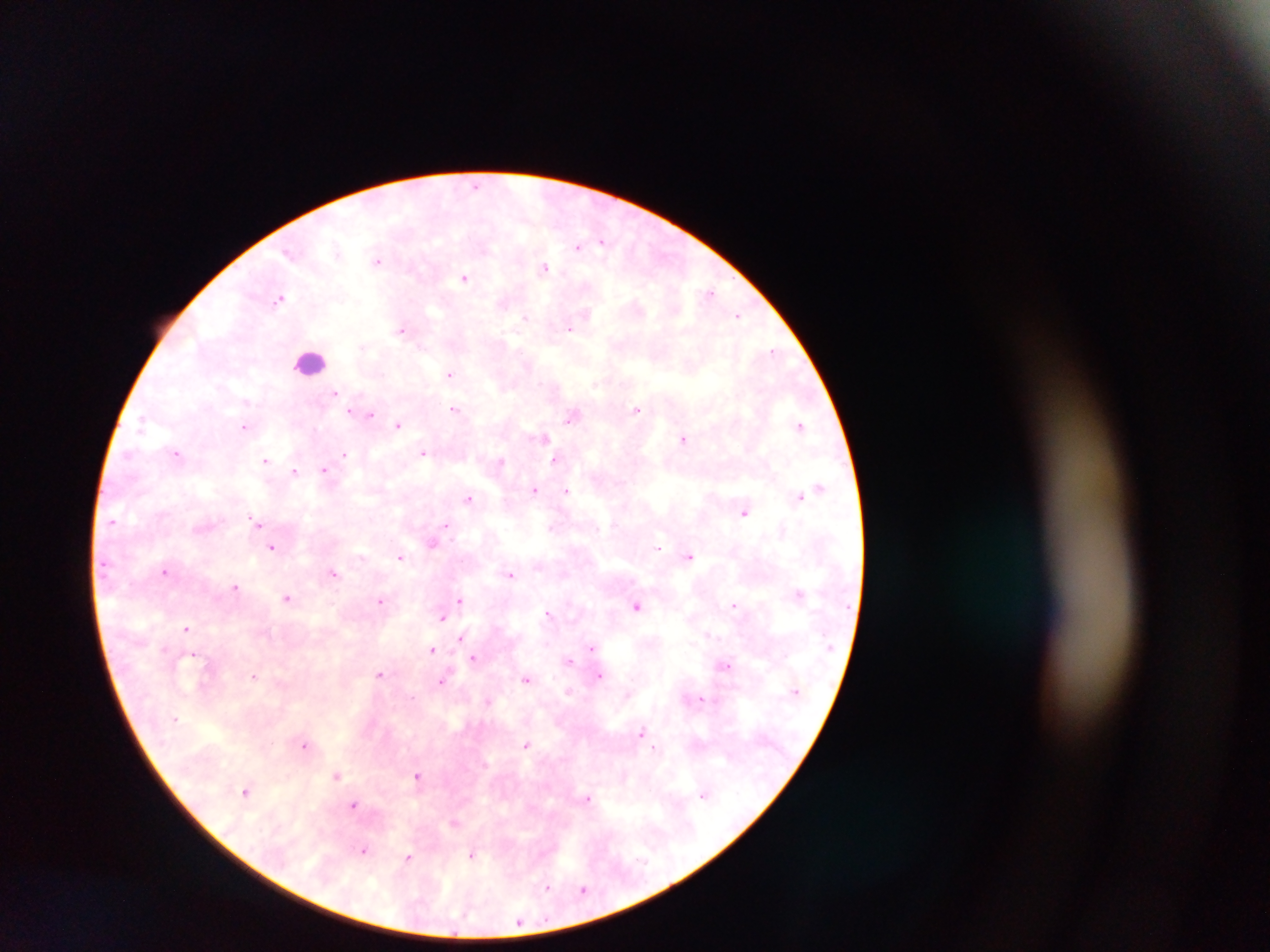

preparation = thick blood smear
country = Ghana
leukocyte locations = approximate centers as {x, y} in pixels: {310, 360}
malaria parasite locations = approximate centers as {x, y} in pixels: {476, 184}, {603, 241}, {578, 246}, {378, 260}, {545, 267}, {464, 277}, {710, 293}, {280, 298}, {737, 315}, {527, 317}, {570, 327}, {403, 328}, {774, 350}, {450, 373}, {336, 393}, {637, 408}, {455, 409}, {355, 412}, {369, 414}, {574, 417}, {399, 424}, {800, 426}, {245, 427}, {543, 437}, {685, 439}, {177, 452}, {424, 453}, {345, 455}, {557, 460}, {266, 461}, {501, 462}, {325, 470}, {295, 471}, {820, 487}, {535, 489}, {567, 491}, {800, 495}, {469, 499}, {744, 512}, {257, 522}, {447, 526}, {433, 542}, {273, 546}, {658, 547}, {401, 556}, {690, 556}, {165, 571}, {334, 573}, {511, 574}, {236, 586}, {799, 593}, {288, 597}, {381, 600}, {460, 600}, {734, 604}, {638, 606}, {549, 614}, {443, 616}, {187, 629}, {462, 638}, {592, 647}, {432, 649}, {193, 653}, {474, 658}, {569, 661}, {725, 664}, {381, 674}, {255, 675}, {600, 675}, {527, 678}, {442, 681}, {569, 691}, {701, 699}, {488, 700}, {642, 732}, {527, 744}, {306, 745}, {655, 748}, {337, 774}, {418, 774}, {246, 790}, {705, 794}, {588, 798}, {354, 805}, {455, 822}, {364, 850}, {473, 854}, {408, 857}, {547, 888}, {584, 889}, {519, 922}
image size = 1270×952 pixels
capture = mobile-phone photograph through a microscope
field of view = single